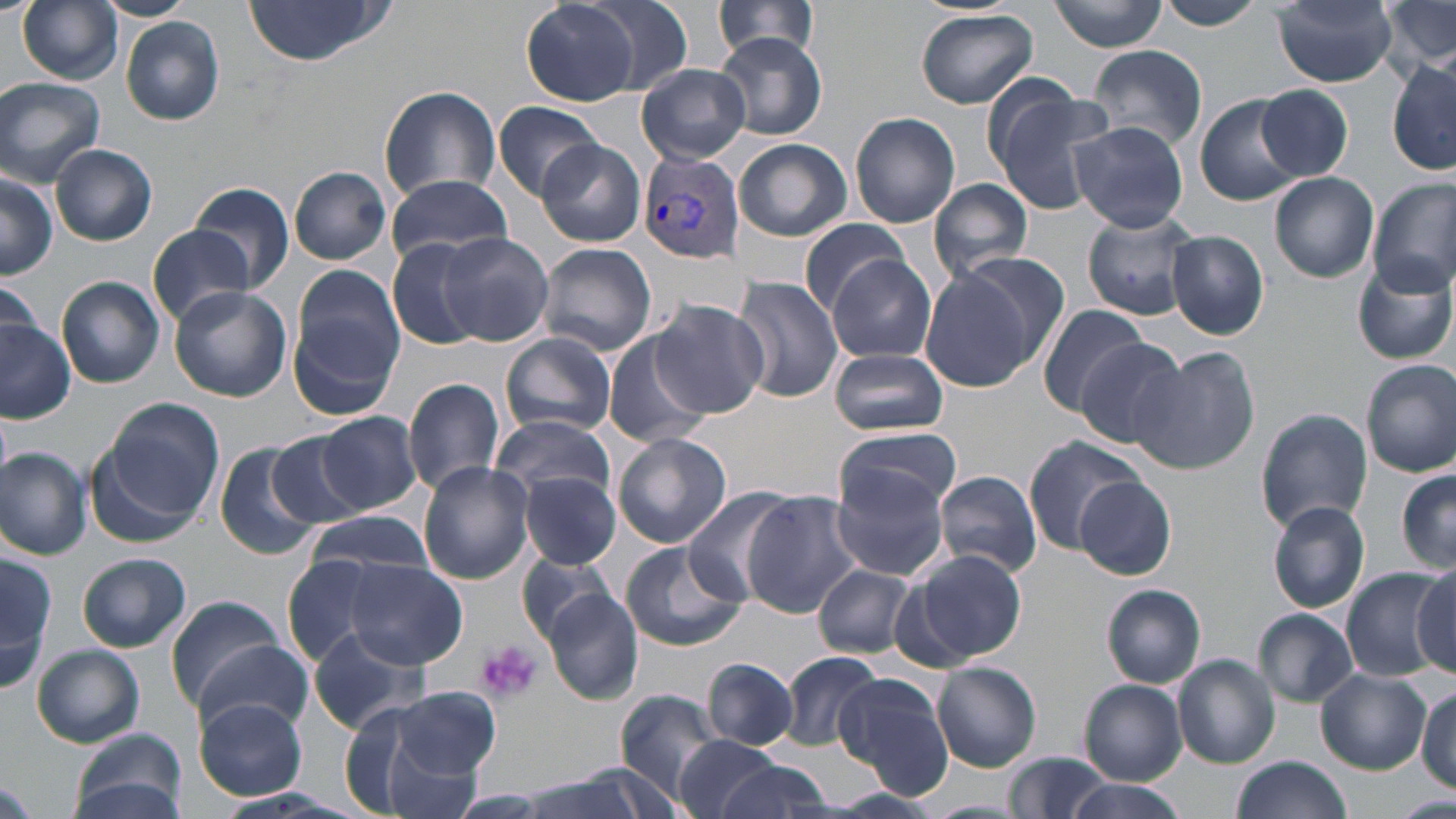

Approximate bounding boxes as [x1, y1, x2, y2] in pixels. Platelet locations: [477, 642, 542, 703]. Plasmodium vivax-infected red blood cell locations: [639, 151, 744, 267]. Uninfected red blood cell locations: [17, 0, 125, 85], [96, 0, 201, 22], [519, 0, 644, 106], [1161, 0, 1263, 31], [242, 1, 390, 67], [711, 1, 822, 63], [1051, 1, 1167, 52], [1382, 1, 1455, 74], [581, 2, 697, 96], [1273, 2, 1397, 87], [915, 7, 1039, 109], [120, 18, 224, 125], [715, 33, 827, 141], [1090, 44, 1208, 149], [1387, 60, 1455, 175], [636, 63, 751, 164], [0, 76, 106, 185], [981, 81, 1110, 212], [379, 84, 500, 203], [1257, 85, 1353, 182], [1195, 96, 1304, 205], [493, 100, 602, 202], [849, 112, 961, 228], [1069, 120, 1190, 234], [734, 138, 851, 242], [536, 140, 646, 246], [52, 145, 157, 246], [289, 165, 391, 266], [0, 171, 57, 280], [384, 173, 513, 268], [1269, 173, 1378, 283], [929, 178, 1036, 282], [1369, 180, 1456, 294], [192, 182, 294, 288], [1082, 211, 1202, 320], [797, 222, 913, 316], [147, 225, 258, 326], [437, 231, 555, 348], [1167, 231, 1268, 340], [388, 239, 490, 350], [537, 243, 657, 357], [826, 255, 938, 362], [1351, 259, 1456, 367], [918, 261, 1048, 391], [0, 275, 49, 364], [732, 275, 843, 404], [56, 277, 166, 388], [287, 277, 403, 419], [167, 284, 291, 402], [651, 300, 768, 417], [1038, 302, 1151, 417], [0, 321, 75, 422], [604, 334, 711, 449], [501, 335, 618, 437], [1073, 337, 1191, 454], [1130, 347, 1261, 475], [829, 348, 948, 437], [1361, 360, 1456, 478], [403, 376, 505, 497], [101, 398, 222, 524], [1255, 407, 1373, 533], [315, 411, 421, 516], [490, 414, 616, 504], [837, 425, 962, 518], [612, 431, 731, 549], [264, 433, 367, 528], [1024, 437, 1139, 551], [213, 442, 328, 562], [89, 446, 197, 548], [0, 448, 92, 559], [416, 461, 534, 585], [830, 468, 951, 581], [934, 469, 1044, 577], [1397, 470, 1455, 573], [520, 472, 621, 570], [1077, 476, 1177, 579], [684, 486, 800, 604], [743, 492, 867, 615], [1267, 500, 1371, 614], [306, 511, 438, 579], [621, 540, 747, 652], [0, 547, 52, 690], [910, 549, 1027, 665], [515, 552, 623, 647], [79, 553, 191, 651], [283, 555, 388, 668], [344, 561, 468, 668], [814, 563, 916, 659], [1341, 567, 1451, 682], [1412, 567, 1455, 674], [1102, 584, 1206, 688], [1088, 586, 1197, 781], [542, 588, 643, 705], [166, 593, 289, 712], [1254, 609, 1358, 706], [309, 627, 432, 733], [194, 639, 314, 734], [32, 646, 144, 748], [777, 650, 883, 753], [1173, 654, 1281, 768], [703, 659, 798, 749], [932, 661, 1042, 771], [1315, 667, 1433, 776], [833, 674, 951, 797], [1079, 680, 1187, 784], [1416, 687, 1455, 792], [390, 688, 501, 780], [612, 690, 727, 799], [195, 698, 307, 800], [356, 704, 493, 817], [69, 730, 187, 819], [673, 734, 785, 819], [1004, 752, 1112, 819], [1233, 755, 1351, 818], [715, 761, 834, 817], [515, 771, 657, 819], [0, 776, 38, 818], [1061, 779, 1188, 819], [1393, 794, 1456, 819], [919, 800, 1028, 817]. Slide-level diagnosis: Plasmodium vivax. Thin blood film. Image is 1456×819 pixels. Captured at 1000x magnification. Optical microscopy. One field of a larger specimen. May-Grünwald-Giemsa-stained preparation.